Assess this cell for malaria.
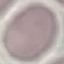

It is uninfected.

{
  "capture": "smartphone through the microscope eyepiece",
  "stain": "Giemsa",
  "preparation": "thin blood film",
  "image_type": "cell patch, automatically extracted from a larger field of view and resized to 64 × 64 pixels"
}